Locate and identify every blood parasite.
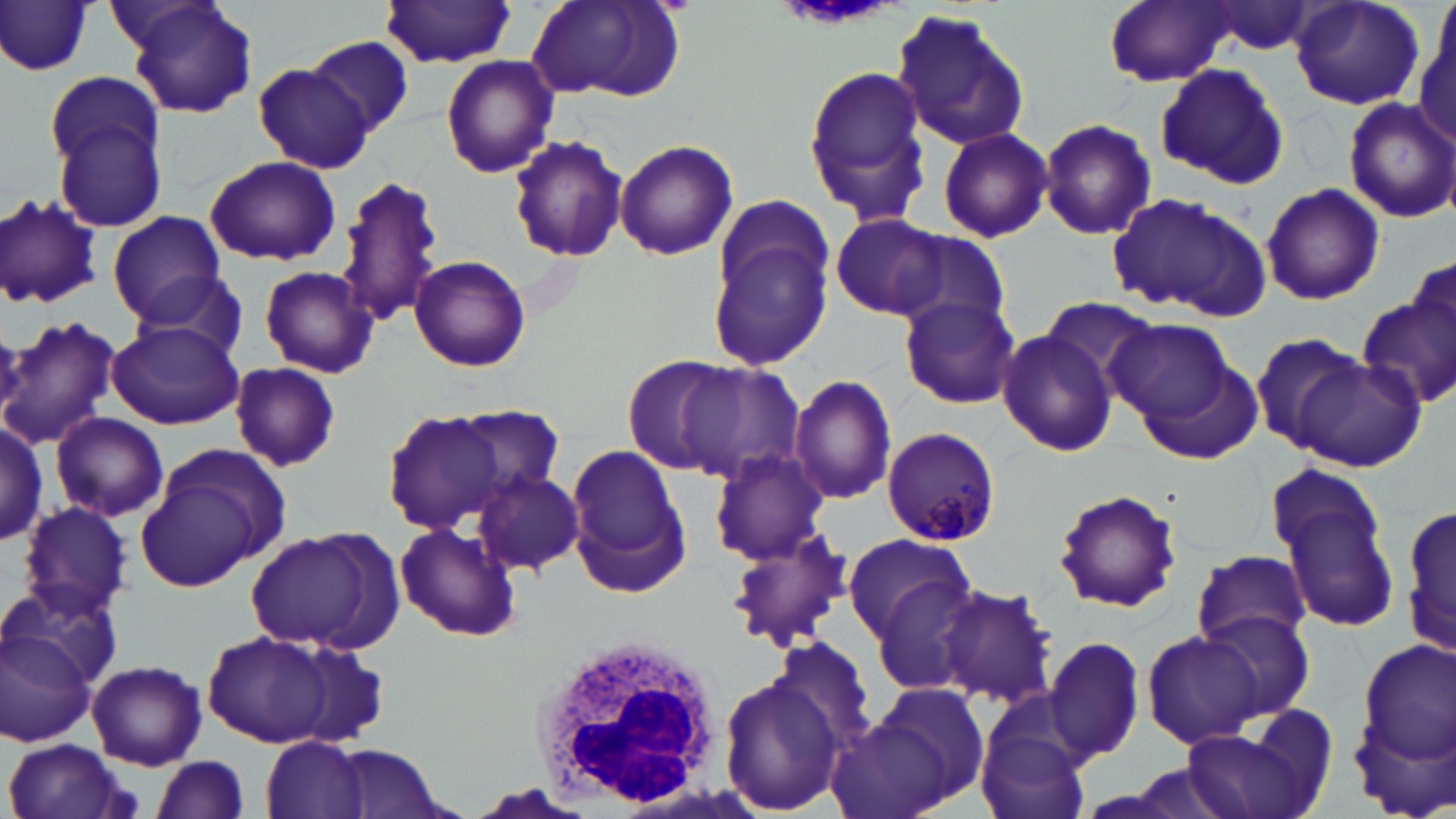

Approximate bounding boxes as [x1, y1, x2, y2] in pixels.
Plasmodium malariae-infected red blood cells: [882, 429, 1002, 546].
No Plasmodium falciparum, Plasmodium ovale, Plasmodium vivax, Babesia divergens, or Trypanosoma brucei observed.

White blood cell locations: [534, 630, 728, 810]. Uninfected red blood cell locations: [120, 0, 260, 120], [525, 0, 686, 104], [1102, 0, 1240, 86], [1288, 1, 1424, 110], [377, 2, 517, 66], [1198, 2, 1323, 56], [0, 4, 95, 78], [890, 9, 1031, 150], [1412, 13, 1454, 146], [308, 36, 413, 139], [441, 54, 557, 177], [800, 59, 934, 228], [253, 63, 375, 172], [1155, 64, 1287, 187], [45, 72, 166, 183], [1343, 98, 1455, 221], [52, 115, 169, 233], [1038, 118, 1157, 241], [936, 125, 1053, 242], [509, 135, 629, 262], [615, 138, 739, 261], [204, 156, 340, 267], [334, 175, 445, 329], [1259, 182, 1385, 304], [1104, 192, 1270, 319], [712, 193, 832, 296], [0, 195, 106, 311], [109, 211, 225, 324], [829, 214, 951, 318], [894, 229, 1014, 333], [707, 233, 833, 373], [410, 253, 531, 372], [1410, 253, 1455, 371], [260, 265, 379, 378], [130, 271, 252, 367], [1356, 288, 1456, 414], [1034, 294, 1164, 404], [898, 295, 1020, 410], [0, 313, 123, 450], [106, 319, 242, 431], [1108, 319, 1234, 424], [997, 324, 1119, 458], [1250, 331, 1369, 452], [1290, 353, 1427, 473], [624, 356, 736, 473], [674, 361, 806, 486], [228, 362, 342, 471], [791, 374, 899, 507], [448, 404, 565, 501], [383, 411, 513, 535], [52, 412, 169, 523], [0, 420, 48, 545], [562, 444, 691, 593], [137, 447, 288, 589], [708, 449, 830, 564], [1267, 464, 1402, 638], [472, 470, 585, 576], [1053, 490, 1182, 613], [17, 500, 135, 619], [1402, 501, 1456, 659], [394, 522, 523, 642], [726, 524, 855, 653], [243, 530, 397, 653], [842, 532, 974, 642], [1189, 549, 1312, 653], [867, 574, 986, 698], [3, 581, 124, 692], [936, 584, 1058, 710], [1198, 611, 1315, 722], [0, 623, 96, 747], [204, 630, 340, 747], [1140, 631, 1264, 751], [772, 635, 879, 755], [1045, 635, 1147, 762], [1354, 635, 1455, 780], [279, 641, 393, 749], [87, 659, 207, 769], [720, 672, 841, 817], [871, 685, 989, 805], [826, 716, 953, 819], [1182, 721, 1322, 819], [975, 724, 1090, 819], [261, 736, 371, 819], [4, 737, 131, 819], [329, 745, 447, 819], [149, 757, 251, 819]. Slide-level diagnosis: Plasmodium malariae. Light microscopy. One field of a larger specimen. May-Grünwald-Giemsa-stained preparation. Image is 1456×819 pixels. Thin blood film. 1000x magnification.